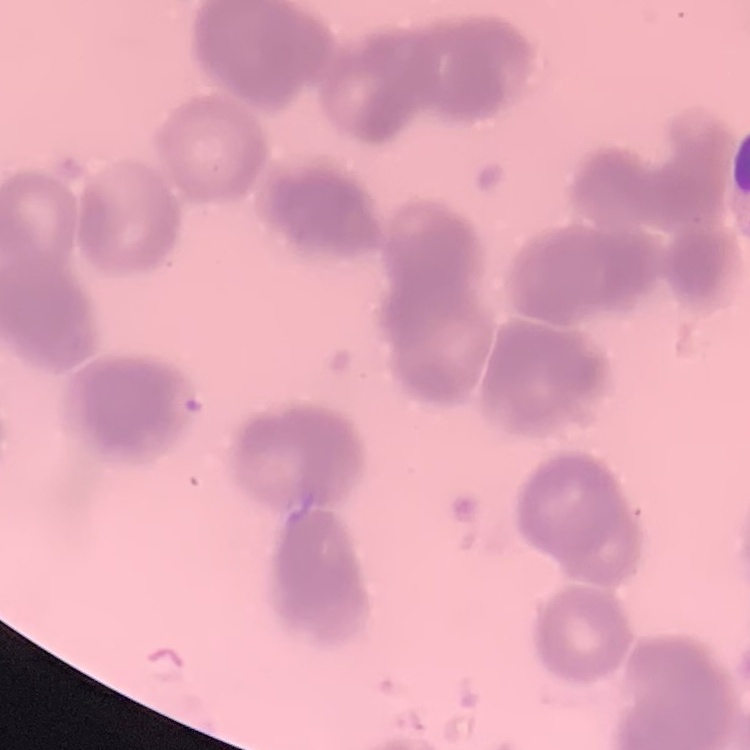
red blood cell morphology = rouleaux formation
stain = Field's or Giemsa
image type = square crop of a larger photomicrograph
preparation = thin peripheral smear